State which parasite is depicted.
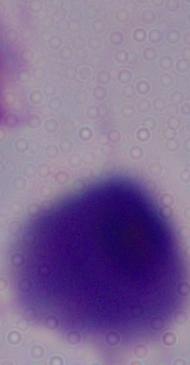

A trichomonad.

modality = micrograph
magnification = 1000x